Locate every Plasmodium malariae-infected red blood cell.
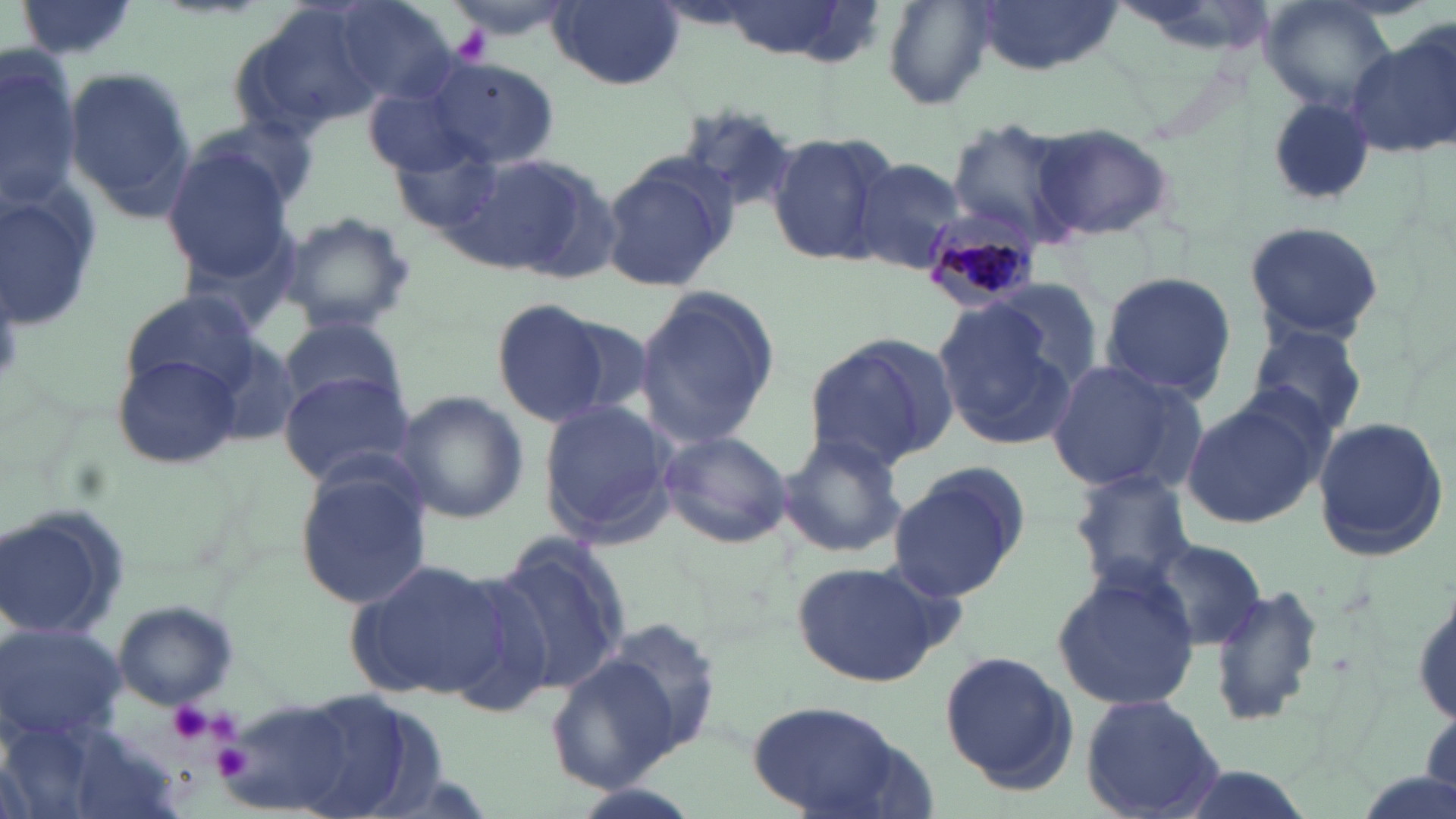

Approximate bounding boxes as named x1/y1/x2/y2 corners in pixels.
Plasmodium malariae-infected red blood cells: (x1=919, y1=211, x2=1042, y2=312).

Summary:
  - Uninfected red blood cell locations: (x1=14, y1=0, x2=145, y2=65), (x1=440, y1=0, x2=576, y2=40), (x1=972, y1=0, x2=1117, y2=76), (x1=1260, y1=0, x2=1399, y2=115), (x1=548, y1=1, x2=682, y2=89), (x1=330, y1=2, x2=459, y2=104), (x1=881, y1=2, x2=997, y2=109), (x1=226, y1=5, x2=387, y2=138), (x1=1350, y1=28, x2=1456, y2=160), (x1=0, y1=52, x2=83, y2=206), (x1=423, y1=58, x2=560, y2=168), (x1=65, y1=66, x2=198, y2=219), (x1=1265, y1=97, x2=1377, y2=207), (x1=189, y1=111, x2=323, y2=222), (x1=944, y1=117, x2=1084, y2=245), (x1=1028, y1=123, x2=1178, y2=244), (x1=766, y1=129, x2=899, y2=269), (x1=390, y1=136, x2=506, y2=232), (x1=163, y1=145, x2=298, y2=282), (x1=465, y1=153, x2=616, y2=284), (x1=600, y1=155, x2=734, y2=293), (x1=849, y1=156, x2=969, y2=279), (x1=1, y1=180, x2=104, y2=338), (x1=276, y1=210, x2=418, y2=335), (x1=1242, y1=219, x2=1387, y2=344), (x1=1098, y1=271, x2=1238, y2=401), (x1=987, y1=279, x2=1104, y2=392), (x1=632, y1=283, x2=781, y2=451), (x1=121, y1=290, x2=260, y2=402), (x1=493, y1=299, x2=609, y2=428), (x1=933, y1=301, x2=1075, y2=452), (x1=279, y1=313, x2=407, y2=414), (x1=555, y1=315, x2=657, y2=421), (x1=1242, y1=323, x2=1373, y2=438), (x1=804, y1=333, x2=959, y2=470), (x1=202, y1=336, x2=304, y2=447), (x1=111, y1=352, x2=242, y2=470), (x1=1041, y1=357, x2=1200, y2=497), (x1=278, y1=370, x2=416, y2=487), (x1=394, y1=390, x2=529, y2=524), (x1=1180, y1=395, x2=1326, y2=531), (x1=537, y1=400, x2=675, y2=546), (x1=1308, y1=415, x2=1448, y2=559), (x1=657, y1=429, x2=792, y2=548), (x1=774, y1=433, x2=909, y2=561), (x1=887, y1=462, x2=1029, y2=603), (x1=292, y1=465, x2=432, y2=611), (x1=1068, y1=471, x2=1197, y2=592), (x1=2, y1=504, x2=131, y2=641), (x1=493, y1=533, x2=631, y2=697), (x1=1149, y1=539, x2=1265, y2=651), (x1=347, y1=555, x2=504, y2=699), (x1=787, y1=561, x2=951, y2=686), (x1=1049, y1=565, x2=1201, y2=716), (x1=432, y1=571, x2=560, y2=719), (x1=1206, y1=586, x2=1324, y2=728), (x1=1412, y1=592, x2=1455, y2=729), (x1=111, y1=600, x2=240, y2=711), (x1=598, y1=614, x2=725, y2=758), (x1=0, y1=623, x2=130, y2=746), (x1=940, y1=651, x2=1080, y2=794), (x1=544, y1=654, x2=682, y2=794), (x1=278, y1=685, x2=456, y2=819), (x1=1080, y1=694, x2=1225, y2=818), (x1=745, y1=700, x2=920, y2=818)
  - Platelet locations: (x1=451, y1=24, x2=490, y2=62), (x1=165, y1=701, x2=214, y2=747), (x1=208, y1=713, x2=241, y2=745), (x1=213, y1=743, x2=253, y2=778)
  - Slide-level diagnosis: Plasmodium malariae
  - Image size: 1456×819 pixels
  - Preparation: thin blood film
  - Modality: optical microscopy
  - Stain: May-Grünwald-Giemsa
  - Magnification: 1000x
  - Field of view: one of a larger specimen